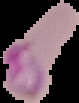
malaria status = parasitized
preparation = thin blood smear
image type = segmented cell region with the area outside set to black
image size = 79×103 pixels